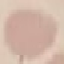

Summary:
  - Malaria status: uninfected
  - Capture: smartphone through the microscope eyepiece
  - Image type: automatically extracted cell patch, resized to 64 × 64 pixels
  - Stain: Giemsa
  - Preparation: thin smear